Give the position of every Plasmodium parasite and every leukocyte.
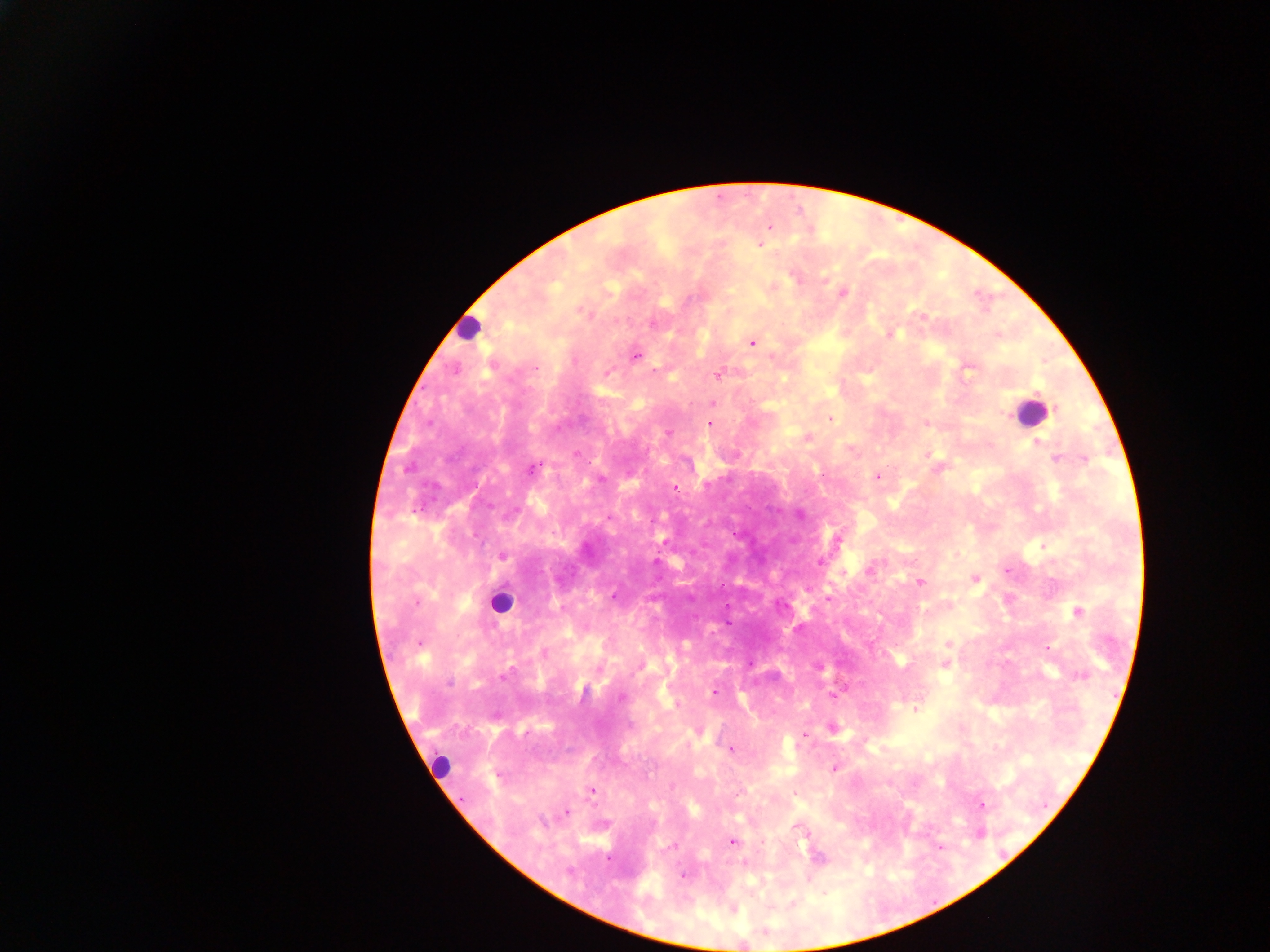
Approximate centers as (x, y) in pixels.
Plasmodium parasites: (769, 228), (760, 244), (796, 278), (825, 280), (843, 293), (585, 314), (923, 317), (653, 324), (890, 335), (752, 342), (635, 357), (536, 368), (455, 369), (654, 371), (606, 373), (717, 375), (712, 404), (1058, 408), (830, 419), (927, 422), (710, 423), (668, 433), (808, 437), (1038, 443), (575, 454), (1056, 458), (1086, 460), (406, 469), (531, 469), (877, 477), (675, 487), (799, 515), (609, 517), (838, 540), (957, 554), (503, 556), (819, 562), (870, 570), (1006, 571), (974, 579), (919, 582), (613, 595), (828, 598), (924, 610), (1078, 611), (729, 624), (948, 644), (1048, 647), (544, 653), (943, 665), (638, 666), (818, 668), (506, 675), (1082, 675), (449, 683), (714, 693), (833, 696), (620, 698), (676, 705), (915, 710), (832, 729), (731, 750), (834, 769), (592, 790), (738, 794), (794, 794), (982, 805), (566, 812), (543, 822), (799, 829), (731, 842), (673, 847), (744, 863), (568, 871), (683, 876), (792, 903).
Leukocytes: (468, 328), (1030, 411), (500, 602), (439, 766).

Sample from Ghana. Mobile-phone photograph taken through the microscope. Image is 1270×952 pixels. Thick blood smear. Single field of view.